Classify this cell by malaria status.
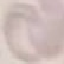
Uninfected.

Summary:
  - Stain: Giemsa
  - Image type: automatically extracted cell patch, resized to 64 × 64 pixels
  - Preparation: thin smear
  - Capture: smartphone camera at the microscope eyepiece